Locate and identify every blood parasite.
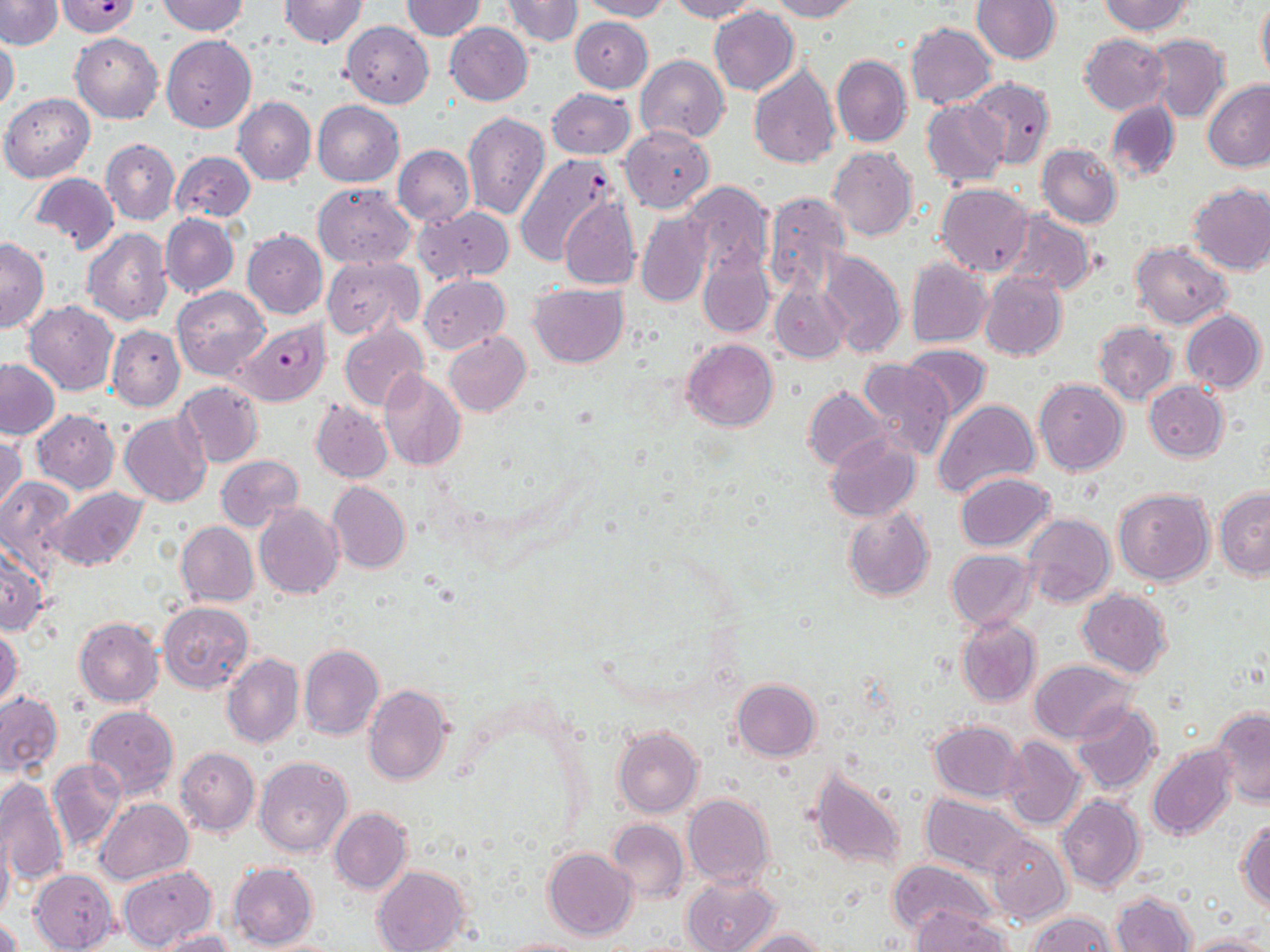

Approximate bounding boxes as (x1,y1)-(x2,y2) corner pairs in pixels.
Plasmodium falciparum-infected red blood cells: (55,0)-(142,37), (514,153)-(620,266), (236,319)-(330,406).
No Plasmodium ovale, Plasmodium malariae, Plasmodium vivax, Babesia divergens, or Trypanosoma brucei observed.

slide_level_diagnosis: Plasmodium falciparum
uninfected_red_blood_cell_locations: 'approximate bounding boxes as (x1,y1)-(x2,y2) corner pairs in pixels: (0,0)-(63,49), (157,0)-(249,36), (279,0)-(368,48), (401,0)-(485,40), (501,0)-(582,45), (577,0)-(673,21), (668,0)-(760,21), (768,0)-(863,21), (971,0)-(1062,65), (1097,0)-(1192,35), (1256,2)-(1270,86), (709,7)-(799,96), (570,16)-(653,92), (342,22)-(434,108), (445,22)-(533,104), (906,23)-(997,109), (70,32)-(163,124), (1142,33)-(1229,123), (1078,34)-(1170,115), (0,35)-(20,116), (162,35)-(257,132), (831,53)-(911,147), (635,55)-(729,141), (749,63)-(841,168), (965,77)-(1055,169), (1203,80)-(1270,172), (547,88)-(636,160), (1,93)-(94,182), (233,96)-(316,185), (921,99)-(1010,189), (1105,99)-(1179,182), (313,100)-(404,186), (462,110)-(549,220), (620,125)-(714,212), (101,139)-(179,226), (1038,143)-(1122,228), (393,145)-(474,226), (827,146)-(917,241), (170,151)-(255,223), (29,173)-(119,256), (683,181)-(774,280), (1186,182)-(1270,274), (313,183)-(415,267), (936,183)-(1034,276), (763,191)-(852,295), (558,195)-(641,290), (414,206)-(514,284), (1002,210)-(1096,295), (635,211)-(712,306), (161,214)-(239,298), (83,229)-(173,326), (242,230)-(327,319), (0,237)-(49,333), (1131,241)-(1233,329), (816,249)-(906,357), (697,250)-(774,338), (322,255)-(423,338), (906,258)-(992,347), (978,270)-(1067,361), (419,275)-(510,353), (770,282)-(850,363), (529,283)-(628,367), (172,286)-(270,381), (24,300)-(119,395), (1181,308)-(1266,392), (1092,321)-(1177,406), (340,324)-(427,411), (107,325)-(184,411), (443,331)-(531,417), (682,338)-(778,431), (900,344)-(992,421), (0,359)-(59,440), (857,359)-(955,462), (378,369)-(465,470), (1034,378)-(1128,475), (175,381)-(264,468), (1144,381)-(1228,461), (803,386)-(890,471), (933,398)-(1040,500), (311,399)-(394,482), (32,410)-(119,492), (120,412)-(210,506), (0,432)-(26,518), (824,433)-(921,521), (216,455)-(303,531), (954,472)-(1055,552), (0,475)-(76,576), (327,482)-(410,575), (47,487)-(147,571), (1113,488)-(1214,585), (1216,488)-(1269,580), (254,503)-(343,599), (843,508)-(934,601), (1022,514)-(1115,608), (176,521)-(259,607), (1,545)-(47,634), (947,550)-(1035,630), (1076,589)-(1173,677), (159,602)-(253,693), (73,617)-(163,707), (956,617)-(1041,708), (0,625)-(23,708), (299,645)-(385,741), (222,653)-(304,750), (320,658)-(418,762), (1030,660)-(1136,743), (731,679)-(821,761), (363,684)-(454,786), (0,691)-(63,777), (1072,703)-(1162,796), (84,704)-(179,798), (1212,707)-(1270,807), (929,720)-(1023,801), (612,726)-(703,818), (1001,736)-(1085,829), (1147,744)-(1237,840), (176,747)-(259,836), (254,756)-(352,858), (48,758)-(127,856), (804,765)-(905,872), (0,777)-(69,887), (682,793)-(774,888), (920,793)-(1027,875), (1057,794)-(1144,895), (96,798)-(193,884), (330,808)-(411,893), (606,818)-(688,904), (1236,819)-(1270,912), (0,826)-(13,926), (985,831)-(1070,924), (543,847)-(637,940), (888,860)-(998,941), (228,861)-(318,950), (373,865)-(471,952), (118,866)-(216,950), (29,869)-(119,952), (683,875)-(779,952), (1112,891)-(1196,952), (912,908)-(1012,952), (1029,911)-(1120,951), (0,919)-(22,952), (737,928)-(830,952), (153,929)-(236,952), (1182,934)-(1267,952), (498,937)-(585,952)'
preparation: thin blood smear
field_of_view: one of a larger specimen
stain: May-Grünwald-Giemsa
image_size: 1270×952 pixels
modality: optical microscopy
magnification: 1000x